Report the malaria status of this cell.
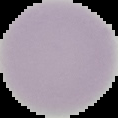

It is uninfected.

Summary:
  - Image size: 118×118 pixels
  - Preparation: thin blood film
  - Image type: segmented cell region on a black background